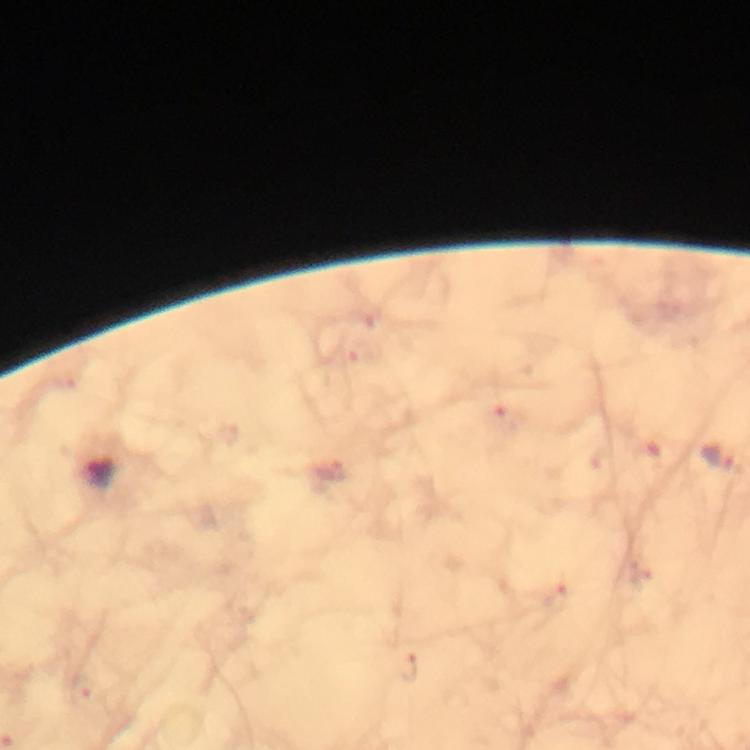

stain = Giemsa
immersion oil = applied
image size = 750×750 pixels
preparation = thick smear
context = from a malaria diagnostic workup
capture = smartphone camera through the microscope
Plasmodium parasite locations = approximate centers as (x, y) in pixels: (720, 459)
cropped from = a single field of view
magnification = 100x